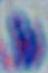
identification = Toxoplasma gondii
modality = micrograph
magnification = 1000x